Point out each Plasmodium parasite.
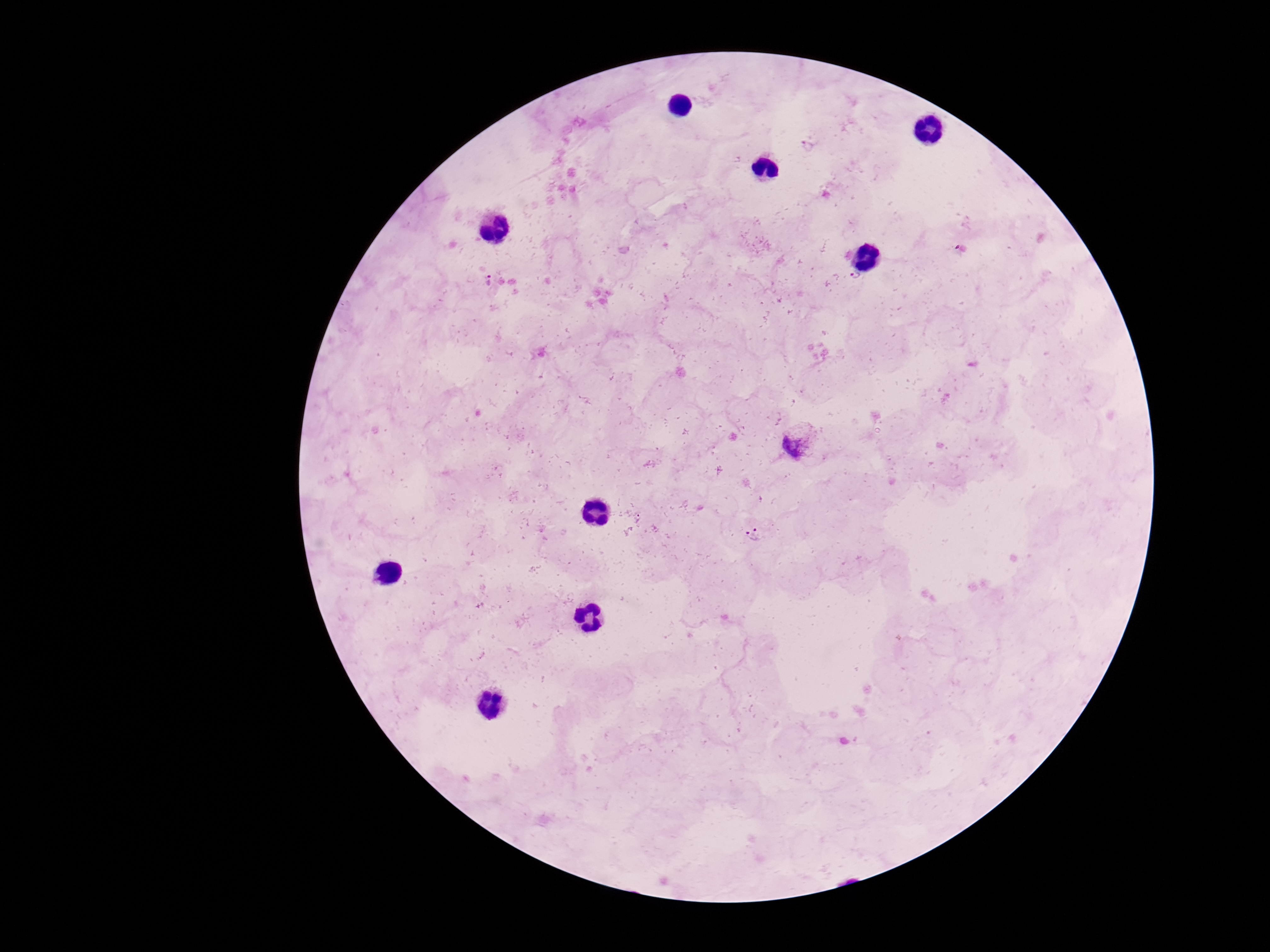

Approximate centers as {x, y} in pixels.
Plasmodium parasites: {808, 146}, {855, 279}, {490, 282}, {800, 442}, {639, 518}, {754, 534}.

{
  "field_of_view": "one from this slide",
  "image_size": "1270×952 pixels",
  "stain": "Giemsa",
  "patient_malaria_status": "infected",
  "magnification": "100x",
  "capture": "smartphone camera through the microscope eyepiece",
  "preparation": "thick blood smear"
}